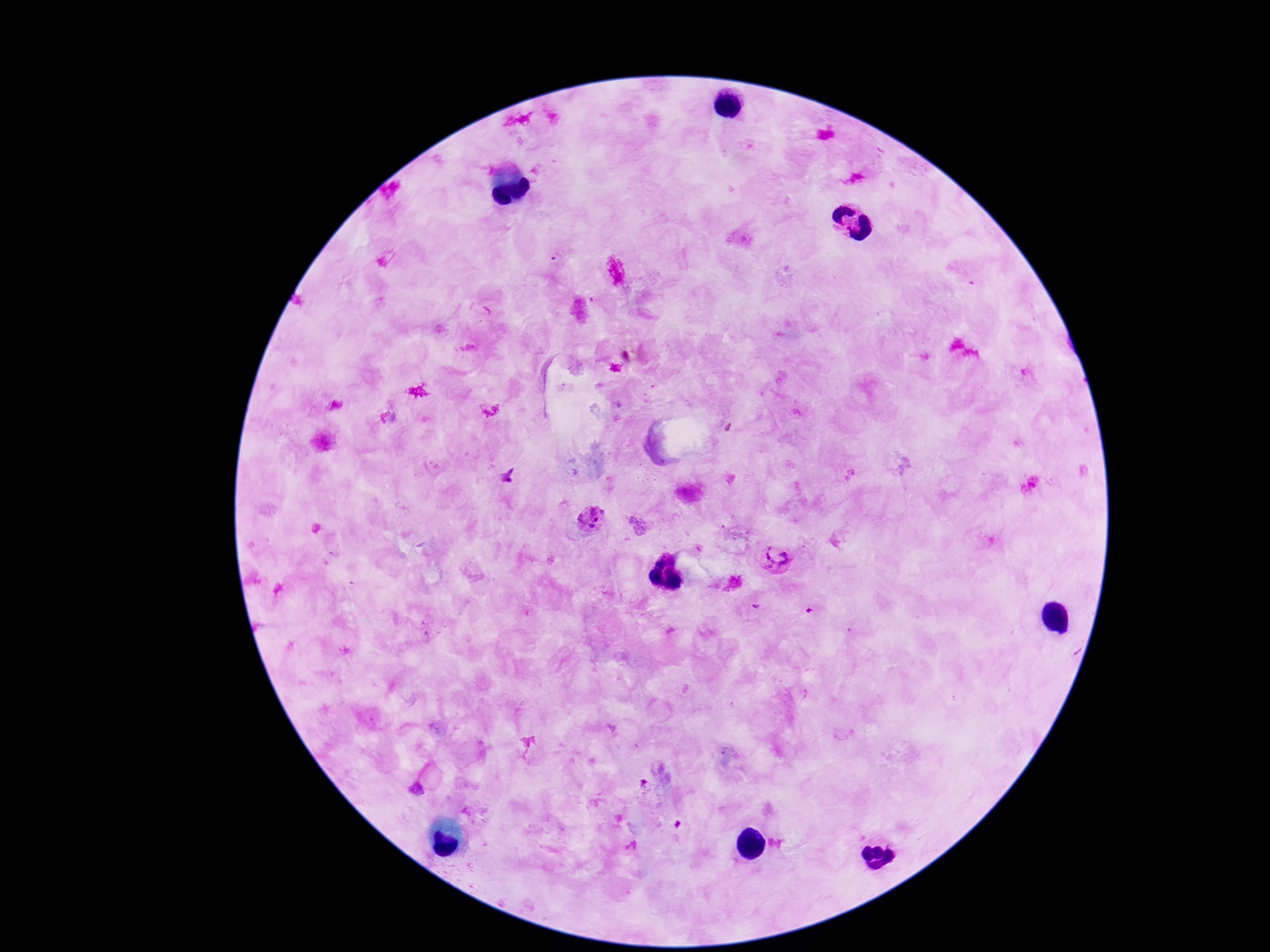
magnification = 100x
preparation = thick peripheral-blood smear
capture = smartphone camera through the microscope eyepiece
Plasmodium parasite locations = approximate centers as {x, y} in pixels: {507, 477}, {591, 518}, {775, 558}, {754, 605}, {417, 790}
image size = 1270×952 pixels
patient malaria status = positive
stain = Giemsa
field of view = single